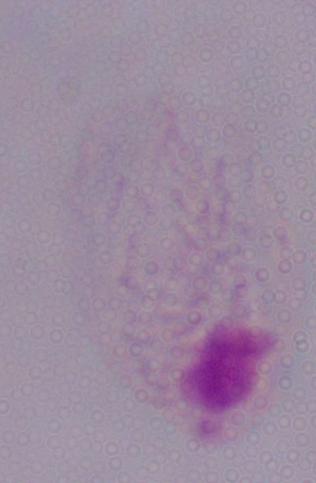 1000x magnification. Photomicrograph. A trichomonad is seen.